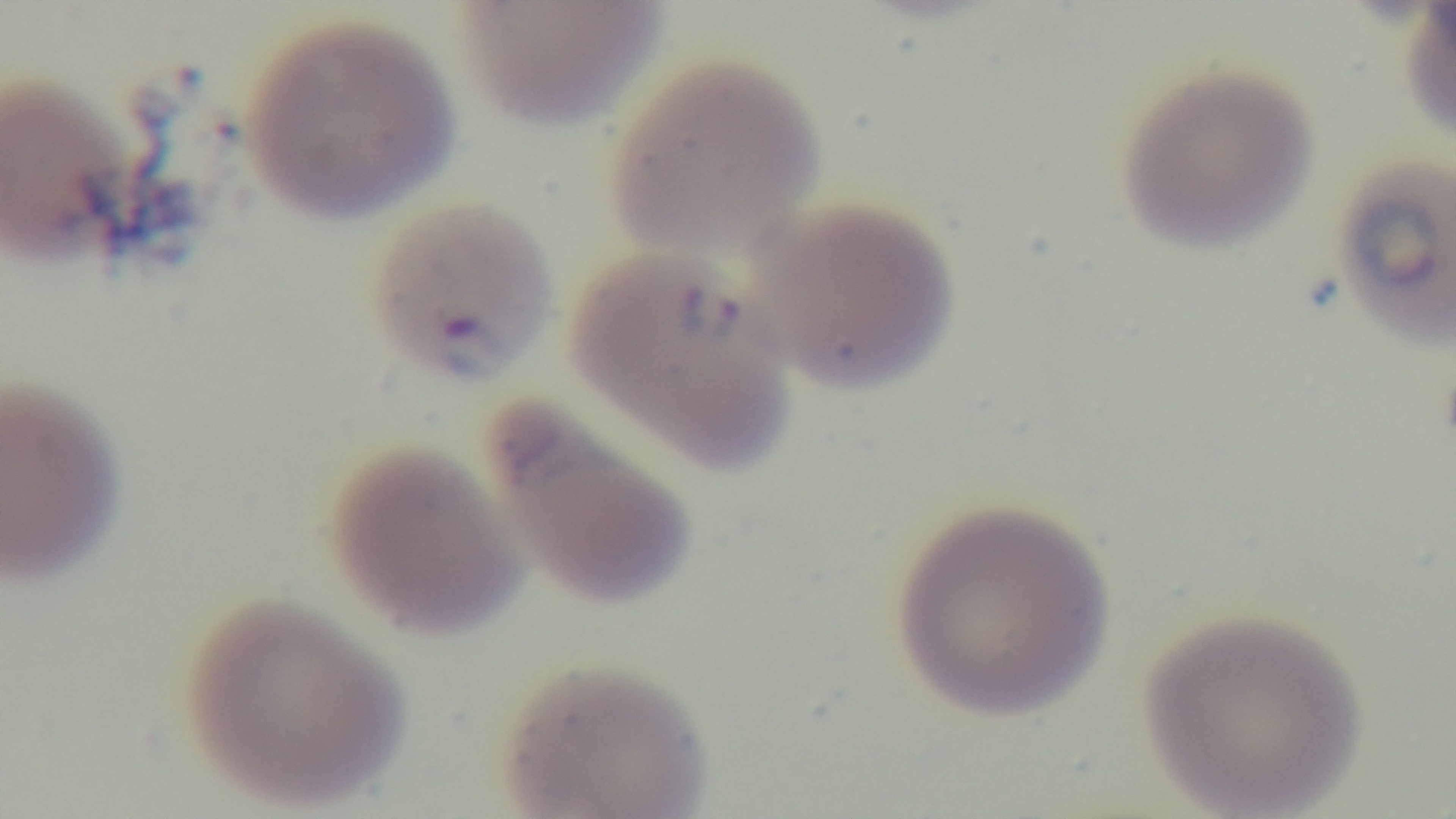
Malaria status: positive. Oil-immersion objective, 100x. Preparation: thin smear. One field from the slide. Light microscopy. Captured with a mounted 4K digital camera. Giemsa-stained.